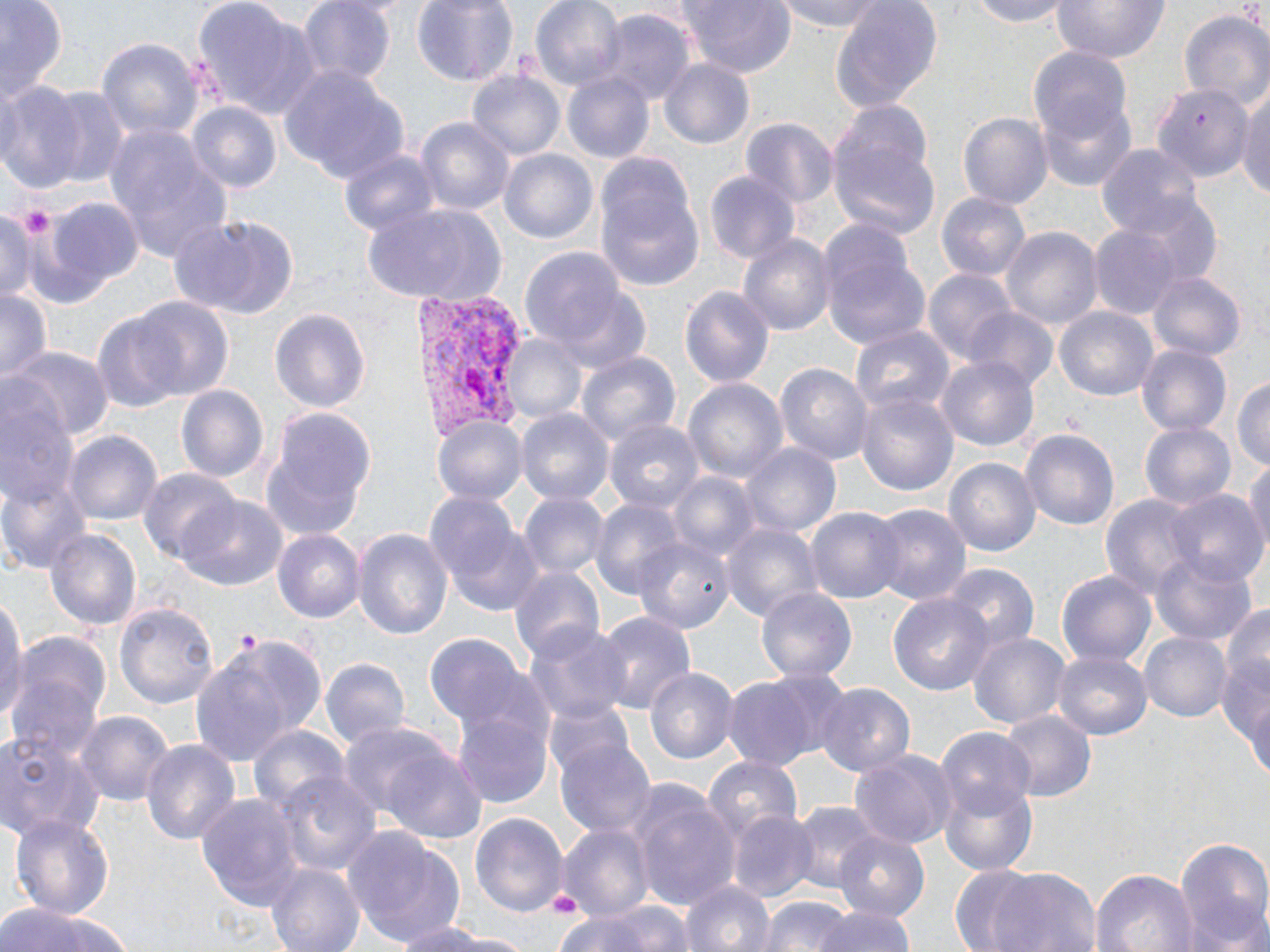
slide-level diagnosis = Plasmodium vivax
preparation = thin blood smear
platelet locations = approximate bounding boxes as (x1, y1, x2, y2) in pixels: (232, 629, 263, 653)
stain = May-Grünwald-Giemsa
magnification = 1000x
uninfected red blood cell locations = approximate bounding boxes as (x1, y1, x2, y2) in pixels: (0, 0, 66, 108), (195, 0, 321, 124), (297, 0, 397, 87), (412, 0, 517, 86), (532, 0, 626, 93), (684, 0, 796, 79), (773, 0, 892, 32), (964, 0, 1076, 30), (1048, 0, 1170, 66), (1235, 0, 1269, 48), (829, 1, 944, 117), (596, 11, 693, 109), (1178, 12, 1270, 108), (98, 37, 201, 147), (1024, 43, 1135, 153), (657, 57, 755, 152), (278, 67, 407, 187), (468, 71, 563, 163), (563, 71, 654, 164), (0, 82, 87, 194), (1152, 83, 1253, 184), (41, 86, 132, 191), (1238, 88, 1270, 205), (1040, 96, 1138, 191), (186, 104, 279, 195), (829, 105, 940, 242), (959, 112, 1052, 208), (416, 117, 513, 220), (741, 117, 839, 214), (105, 122, 233, 269), (1098, 142, 1202, 238), (337, 145, 442, 240), (498, 149, 598, 247), (596, 156, 706, 295), (706, 171, 800, 266), (1118, 191, 1224, 287), (936, 192, 1030, 285), (45, 194, 144, 294), (358, 201, 508, 307), (0, 209, 39, 300), (171, 212, 301, 319), (820, 222, 933, 355), (1089, 224, 1180, 318), (1002, 227, 1102, 333), (737, 231, 836, 341), (519, 246, 630, 356), (924, 268, 1018, 365), (1147, 271, 1246, 362), (542, 275, 653, 373), (677, 285, 776, 389), (0, 286, 51, 389), (132, 297, 234, 402), (270, 304, 373, 415), (1055, 306, 1156, 401), (962, 307, 1058, 394), (91, 313, 188, 414), (848, 324, 955, 421), (501, 333, 588, 424), (1136, 344, 1231, 440), (13, 347, 114, 440), (573, 350, 679, 453), (938, 355, 1039, 453), (774, 361, 874, 464), (1233, 375, 1270, 475), (683, 377, 788, 484), (176, 384, 271, 484), (856, 391, 959, 496), (0, 392, 80, 514), (259, 405, 376, 540), (516, 409, 613, 508), (433, 414, 528, 504), (606, 419, 707, 514), (1139, 420, 1237, 512), (64, 429, 163, 525), (1021, 429, 1121, 533), (741, 443, 842, 538), (945, 456, 1040, 559), (1245, 459, 1270, 558), (139, 469, 239, 565), (669, 472, 763, 566), (0, 478, 91, 573), (1163, 489, 1265, 582), (518, 491, 609, 580), (1099, 491, 1201, 605), (175, 496, 286, 590), (592, 498, 685, 601), (432, 501, 541, 613), (870, 503, 971, 605), (805, 507, 904, 604), (721, 520, 823, 622), (273, 527, 367, 623), (46, 528, 144, 632), (353, 528, 452, 644), (634, 538, 733, 634), (1150, 549, 1255, 647), (942, 564, 1039, 650), (510, 565, 603, 665), (1056, 571, 1155, 668), (757, 587, 857, 683), (889, 592, 993, 696), (1214, 594, 1270, 771), (0, 596, 25, 725), (114, 601, 216, 709), (594, 612, 695, 715), (525, 624, 633, 729), (966, 631, 1071, 734), (1139, 631, 1230, 723), (426, 634, 528, 728), (191, 635, 323, 764), (1053, 648, 1151, 738), (6, 653, 106, 767), (319, 657, 409, 751), (643, 663, 737, 765), (724, 672, 826, 768), (816, 683, 915, 777), (1240, 691, 1270, 783), (453, 707, 553, 810), (74, 709, 175, 808), (997, 709, 1097, 803), (247, 725, 349, 817), (349, 726, 487, 843), (937, 729, 1035, 818), (0, 730, 106, 840), (556, 737, 656, 842), (140, 738, 241, 845), (849, 749, 958, 850), (704, 756, 803, 843), (274, 771, 382, 878), (627, 782, 740, 910), (940, 782, 1039, 876), (196, 793, 304, 914), (788, 803, 882, 897), (728, 809, 820, 901), (471, 810, 568, 922), (9, 813, 115, 923), (556, 825, 651, 919), (341, 827, 468, 949), (833, 831, 932, 923), (1174, 836, 1270, 952), (265, 862, 364, 952), (978, 865, 1102, 952), (1091, 868, 1197, 952), (946, 869, 1053, 951), (682, 876, 774, 952), (756, 896, 854, 952), (556, 900, 699, 952), (0, 901, 135, 952), (810, 906, 922, 952), (389, 919, 523, 950)
image size = 1270×952 pixels
modality = optical microscopy
field of view = one of a larger specimen
Plasmodium vivax-infected red blood cell locations = approximate bounding boxes as (x1, y1, x2, y2) in pixels: (413, 292, 529, 446)